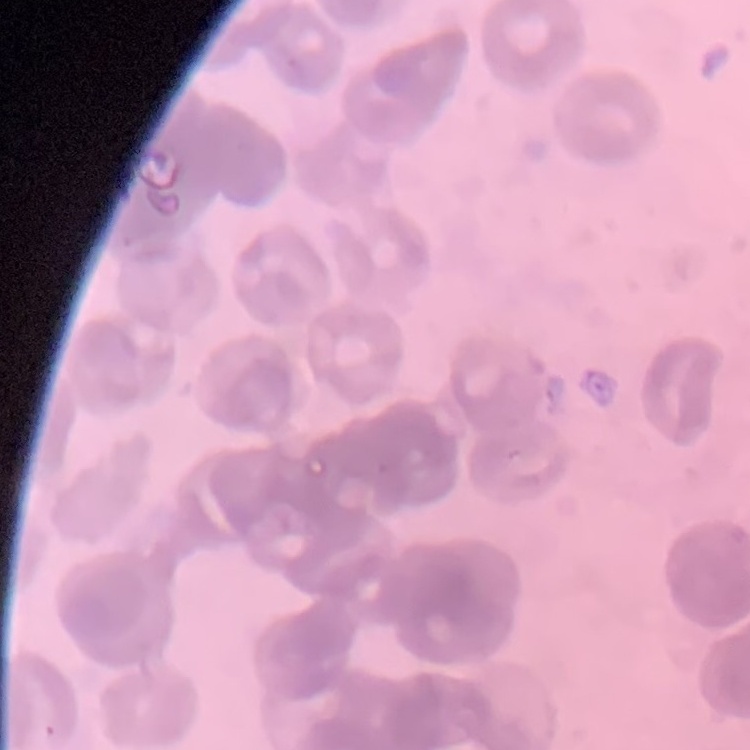
The red blood cells show rouleaux formation. Field's or Giemsa stain. Square crop of a larger photomicrograph. Thin peripheral smear.